Locate every blood parasite and identify its species.
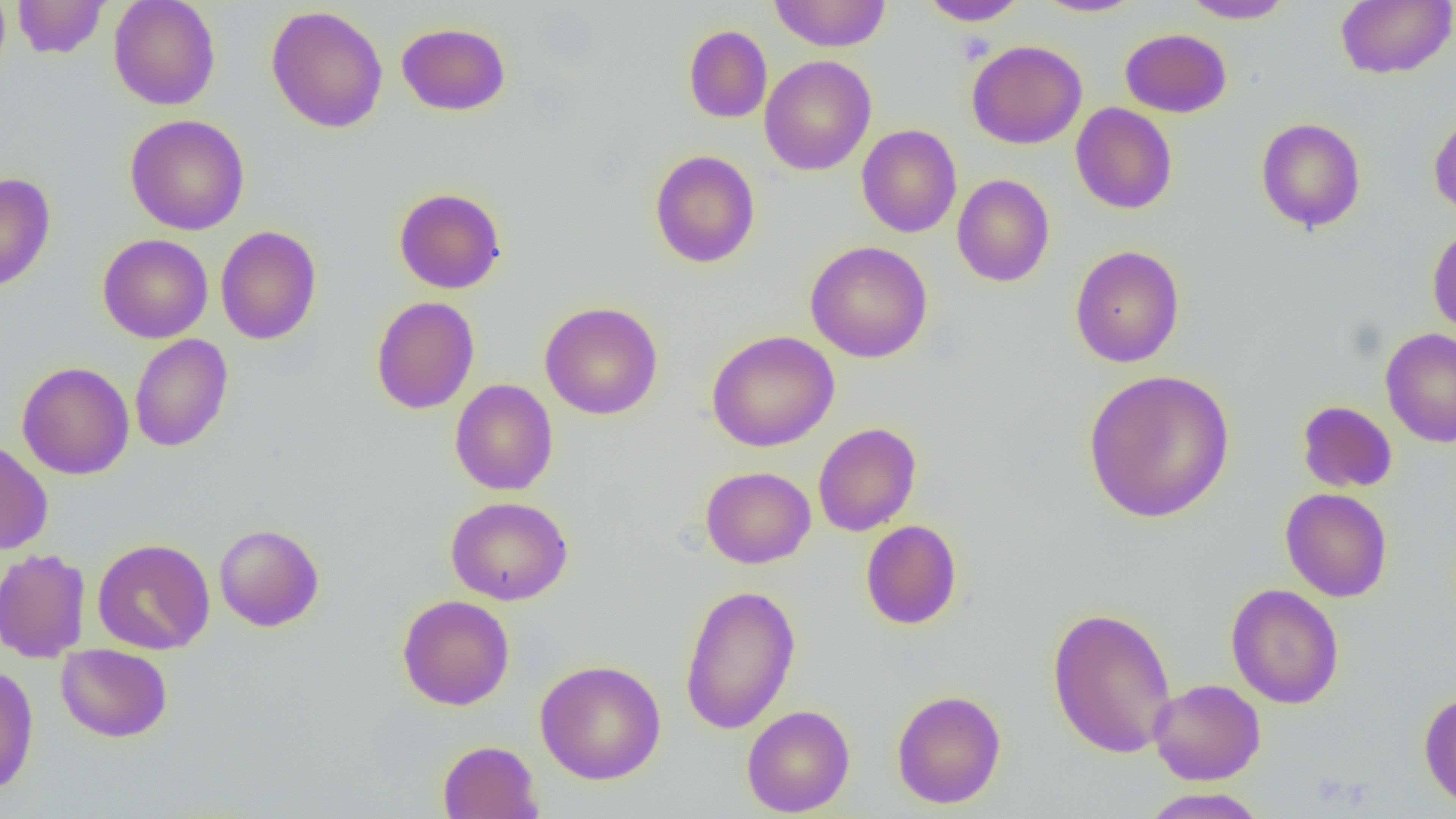
No blood parasites observed.

Approximate bounding boxes as (x1, y1, x2, y2) in pixels. Uninfected red blood cell locations: (12, 0, 109, 58), (109, 0, 221, 110), (769, 0, 891, 52), (918, 0, 1028, 26), (1032, 0, 1144, 17), (1181, 0, 1295, 23), (1335, 0, 1456, 79), (266, 5, 388, 133), (396, 22, 511, 116), (683, 25, 772, 123), (1120, 28, 1232, 118), (967, 40, 1087, 149), (759, 55, 876, 175), (1071, 103, 1177, 214), (1428, 110, 1456, 220), (124, 114, 250, 235), (1256, 117, 1366, 233), (857, 124, 962, 237), (649, 150, 760, 268), (0, 172, 56, 293), (952, 174, 1054, 287), (394, 187, 506, 294), (1427, 224, 1456, 338), (215, 226, 322, 345), (98, 234, 212, 343), (805, 241, 933, 363), (1069, 245, 1184, 368), (370, 296, 480, 415), (539, 301, 663, 420), (1380, 329, 1456, 447), (706, 330, 839, 452), (130, 334, 233, 453), (16, 361, 134, 479), (1082, 369, 1235, 524), (450, 379, 558, 496), (1297, 400, 1397, 492), (813, 422, 921, 536), (0, 439, 53, 555), (701, 466, 815, 568), (1280, 488, 1393, 602), (445, 496, 573, 605), (860, 520, 962, 630), (214, 523, 324, 631), (92, 538, 215, 655), (0, 548, 91, 663), (680, 583, 800, 735), (1226, 583, 1344, 709), (396, 594, 515, 711), (1046, 606, 1177, 758), (56, 644, 173, 742), (535, 659, 666, 784), (0, 665, 39, 795), (1149, 678, 1266, 785), (892, 689, 1006, 808), (1418, 691, 1456, 811), (742, 704, 855, 817), (437, 740, 543, 819), (1139, 788, 1266, 818). Slide-level diagnosis: negative for blood parasites. 1000x magnification. Optical microscopy. Thin blood smear. Image is 1456×819 pixels. One field of a larger specimen.